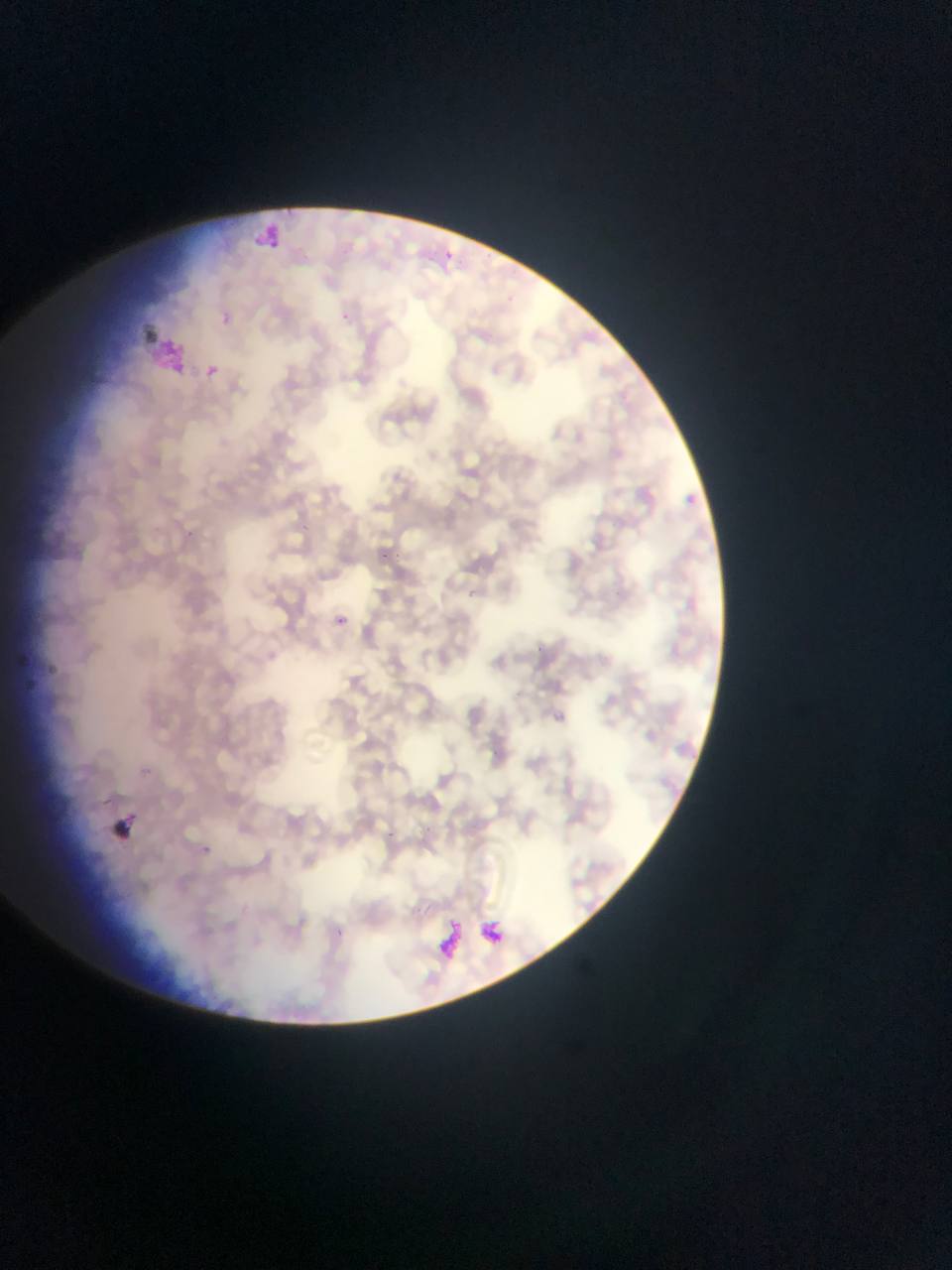
artifact_stain_precipitate_or_debris_locations: 'approximate bounding boxes as left top right bottom in pixels: 251 217 289 258; 137 332 187 393; 101 815 127 851; 425 914 471 970; 479 919 499 947'
image_size: 952×1270 pixels
preparation: thin blood smear
country: Ghana
malaria_parasite_locations: 'approximate bounding boxes as left top right bottom in pixels: 443 249 457 264; 341 313 352 325; 205 365 220 378; 391 473 402 484; 688 484 712 514; 301 521 313 534; 184 526 195 535; 380 548 393 561; 395 551 406 559; 466 587 480 600; 336 616 347 626; 530 640 546 653; 491 750 502 754; 142 766 151 775; 420 824 435 841; 385 827 394 838; 201 844 219 856; 334 927 347 940'
field_of_view: single
capture: mobile-phone photograph through a microscope